Point out each malaria parasite.
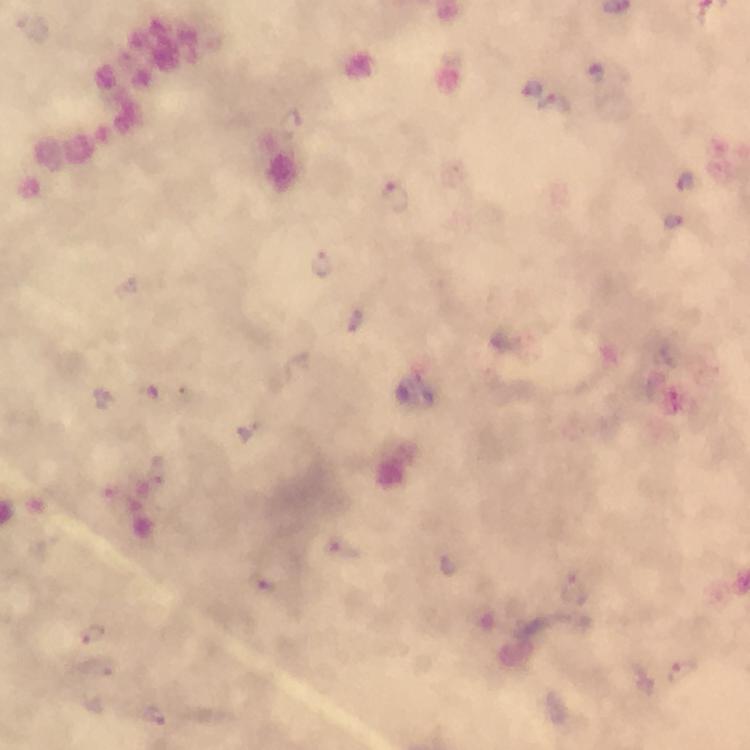
Approximate centers as {x, y} in pixels.
Malaria parasites: {532, 88}, {555, 106}, {290, 122}, {686, 181}, {395, 196}, {322, 264}, {355, 322}, {101, 398}, {341, 546}, {262, 582}, {574, 587}, {93, 634}, {683, 671}, {156, 716}.

Summary:
  - Cropped from: a single field of view
  - Magnification: 100x
  - Capture: smartphone camera through the microscope
  - Stain: Giemsa
  - Preparation: thick smear
  - Context: from a diagnostic examination for malaria
  - Immersion oil: applied
  - Image size: 750×750 pixels